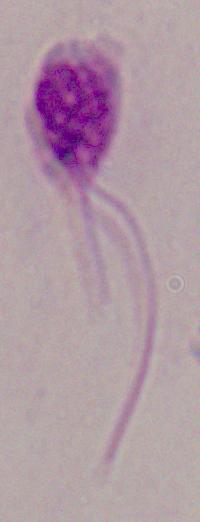
Summary:
  - Identification: Leishmania
  - Modality: photomicrograph
  - Magnification: 1000x